Point out each leukocyte.
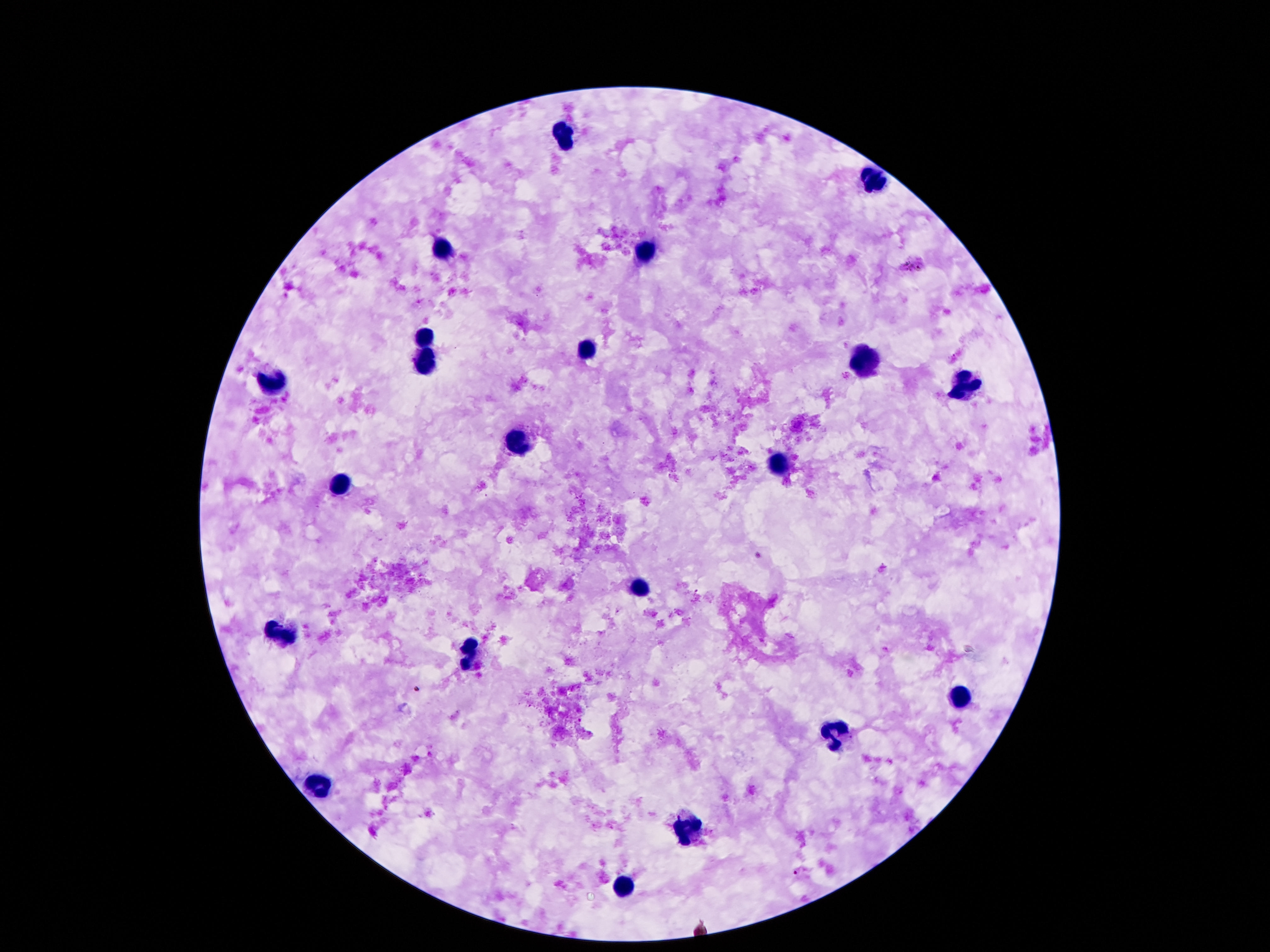

Approximate centers as (x, y) in pixels.
Leukocytes: (563, 134), (872, 178), (444, 251), (641, 257), (424, 337), (584, 350), (864, 361), (422, 367), (270, 376), (965, 386), (516, 446), (780, 464), (344, 483), (639, 587), (277, 634), (473, 653), (961, 699), (834, 735), (322, 783), (686, 829), (623, 887).

image_size: 1270×952 pixels
patient_malaria_status: negative
field_of_view: one from this slide
stain: Giemsa
magnification: 100x
preparation: thick blood film
capture: smartphone camera through the microscope eyepiece